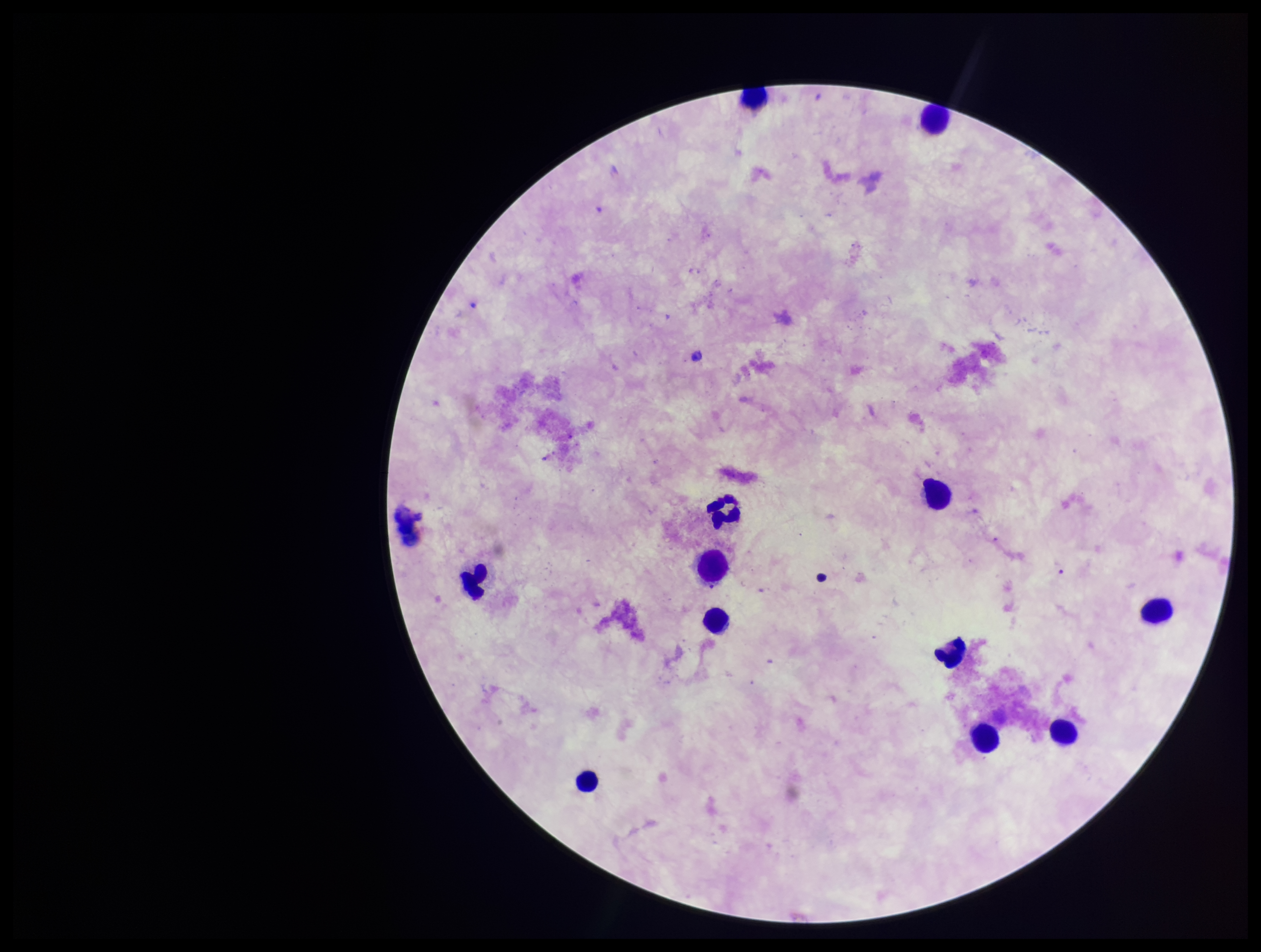

{
  "patient_malaria_status": "negative",
  "plasmodium_parasites": "none detected",
  "capture": "smartphone photograph through the microscope eyepiece",
  "parasite_count": 0,
  "field_of_view": "one from this slide",
  "leukocyte_count": 13,
  "preparation": "thick blood smear",
  "image_size": "1261×952 pixels",
  "stain": "Giemsa"
}